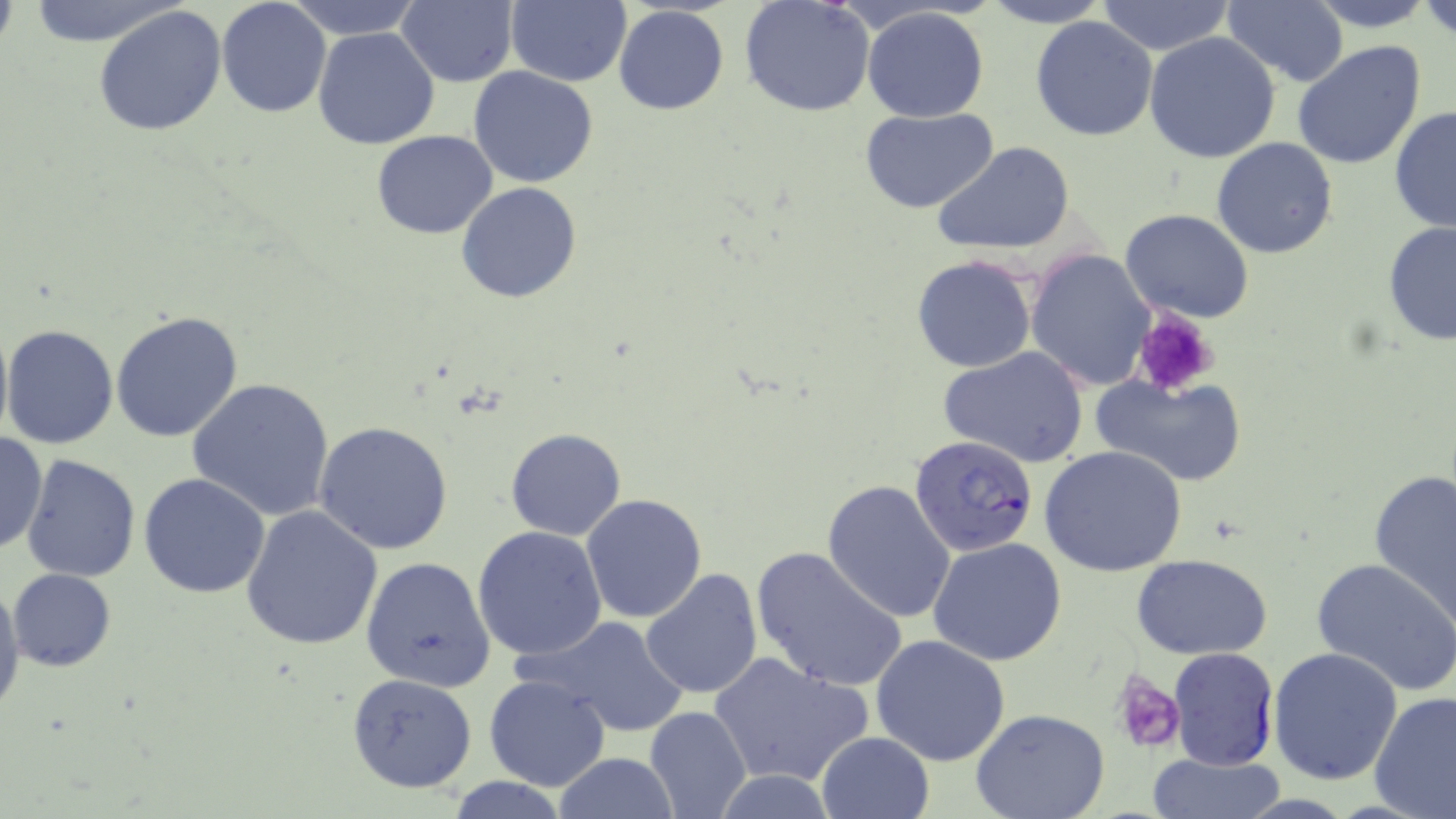
Summary:
  - Coordinate format: approximate bounding boxes as (x1,y1)-(x2,y2) corner pairs in pixels
  - Platelet locations: (1132,307)-(1220,395), (1111,668)-(1185,752)
  - Uninfected red blood cell locations: (17,0)-(185,47), (216,0)-(332,119), (285,0)-(423,39), (739,0)-(876,118), (987,0)-(1109,29), (1301,0)-(1444,30), (1418,0)-(1455,42), (395,1)-(518,87), (503,1)-(632,87), (1096,1)-(1234,54), (1223,2)-(1348,86), (94,4)-(226,139), (612,5)-(731,115), (860,7)-(991,122), (213,13)-(437,130), (1029,14)-(1159,142), (312,27)-(441,150), (1145,32)-(1280,162), (1293,41)-(1427,171), (469,65)-(599,187), (1389,104)-(1456,235), (861,107)-(1000,214), (370,131)-(497,240), (1211,138)-(1339,259), (932,141)-(1076,254), (455,182)-(583,303), (1121,208)-(1254,324), (1381,221)-(1456,346), (1025,247)-(1156,391), (911,254)-(1037,373), (110,312)-(243,443), (3,323)-(118,449), (937,345)-(1090,468), (1091,374)-(1249,488), (188,379)-(337,522), (314,420)-(455,556), (505,428)-(627,540), (0,431)-(48,555), (0,443)-(100,561), (1042,446)-(1187,577), (21,454)-(142,581), (1369,468)-(1456,630), (139,473)-(269,598), (822,480)-(956,623), (581,494)-(708,624), (242,506)-(383,651), (472,526)-(608,663), (927,536)-(1067,666), (751,545)-(909,693), (1131,553)-(1275,659), (360,556)-(496,691), (1312,559)-(1456,695), (8,568)-(116,672), (641,569)-(763,701), (0,580)-(23,713), (524,615)-(688,739), (870,634)-(1011,766), (1267,645)-(1402,784), (709,653)-(870,789), (348,673)-(477,793), (483,674)-(612,792), (1369,690)-(1456,819), (645,705)-(752,819), (971,710)-(1111,819), (816,730)-(936,819), (550,752)-(682,819), (1149,754)-(1283,819), (713,772)-(840,817)
  - Plasmodium falciparum-infected red blood cell locations: (907,435)-(1038,557), (1168,647)-(1280,768)
  - Slide-level diagnosis: Plasmodium falciparum
  - Stain: May-Grünwald-Giemsa
  - Image size: 1456×819 pixels
  - Field of view: one of a larger specimen
  - Magnification: 1000x
  - Modality: light microscopy
  - Preparation: thin blood film